Locate every Plasmodium parasite.
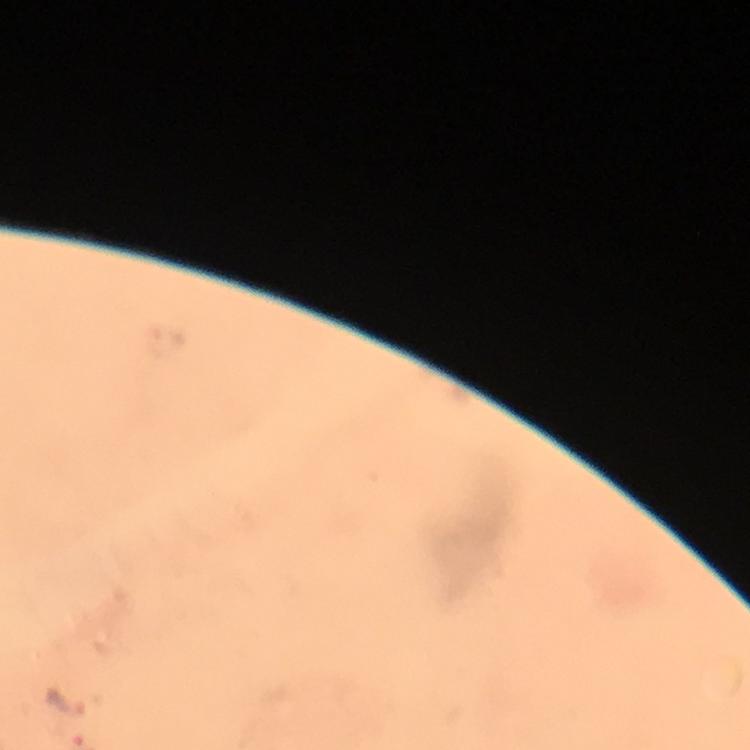

Approximate object centers, in pixels from the top-left corner.
Plasmodium parasites: (x=66, y=702).

At 100x magnification. Thick smear. Photographed through the microscope with a smartphone camera. From a malaria diagnostic workup. Giemsa-stained preparation. Image is 750×750 pixels. Immersion oil applied. A crop from one field of view.